Mark where white blood cells are.
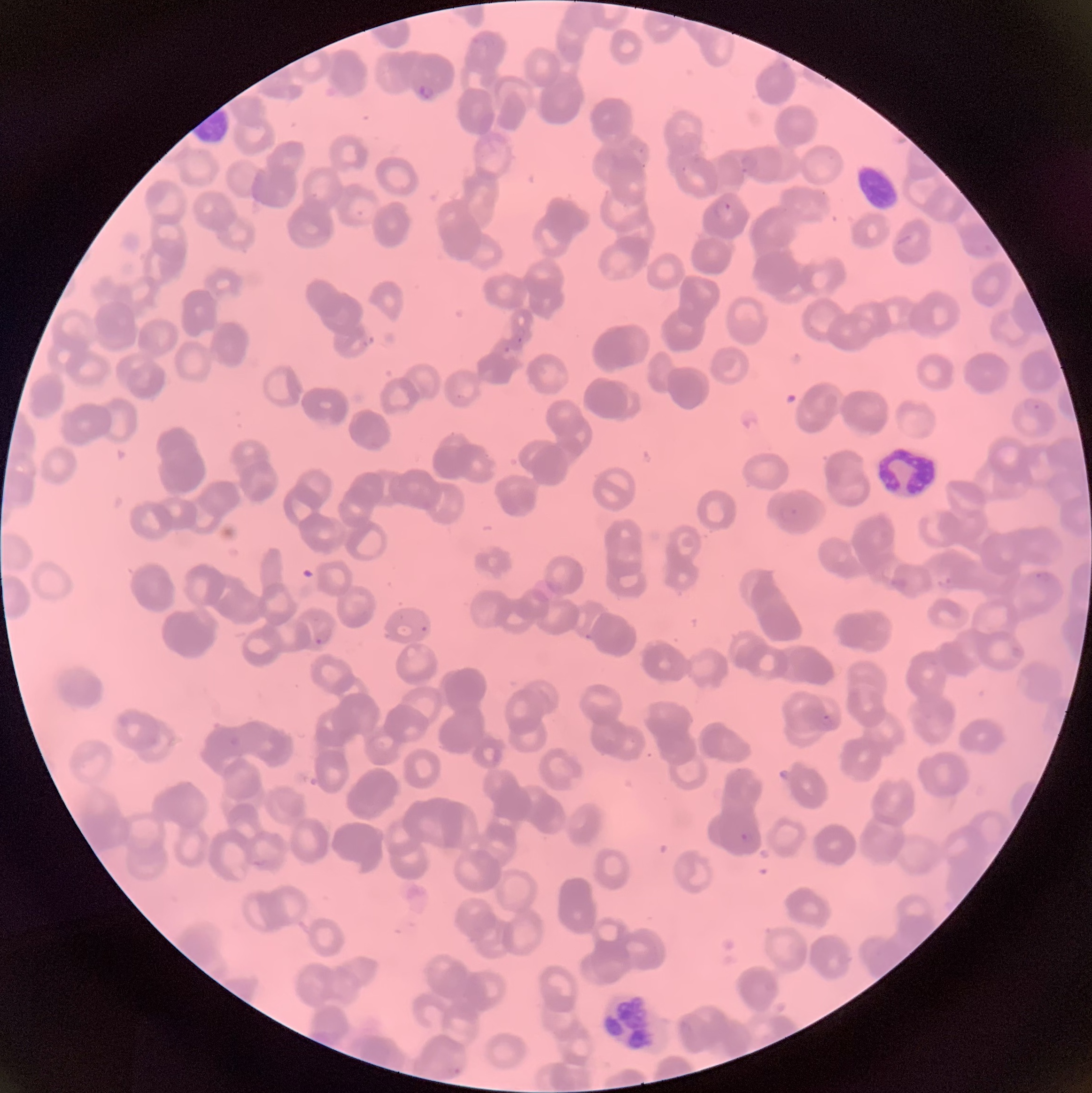

Approximate bounding boxes as named x1/y1/x2/y2 corners in pixels.
White blood cells: (x1=875, y1=445, x2=940, y2=502), (x1=596, y1=990, x2=664, y2=1054).

Plasmodium parasites too small for a box (approximate object centers, named x/y in pixels): (x=520, y=340), (x=424, y=628). Plasmodium parasite locations: (x1=415, y1=83, x2=435, y2=101), (x1=716, y1=200, x2=735, y2=221), (x1=503, y1=345, x2=510, y2=353), (x1=1022, y1=396, x2=1042, y2=413), (x1=314, y1=626, x2=333, y2=645), (x1=822, y1=713, x2=831, y2=720), (x1=739, y1=830, x2=755, y2=843). Thin blood smear. Light microscopy. The red blood cells show rouleaux formation. Image is 1092×1093 pixels.